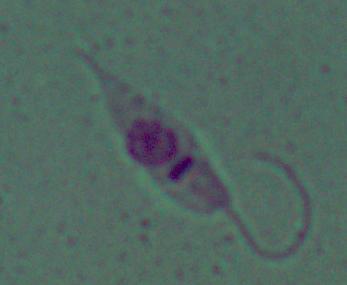

Captured at 1000x magnification. Photomicrograph. A Leishmania parasite is seen.